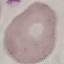

{
  "malaria_status": "uninfected",
  "image_type": "cell patch, automatically extracted from a larger field of view and resized to 64 × 64 pixels",
  "capture": "smartphone through the microscope eyepiece",
  "preparation": "thin blood smear",
  "stain": "Giemsa"
}